Assess for Plasmodium parasites.
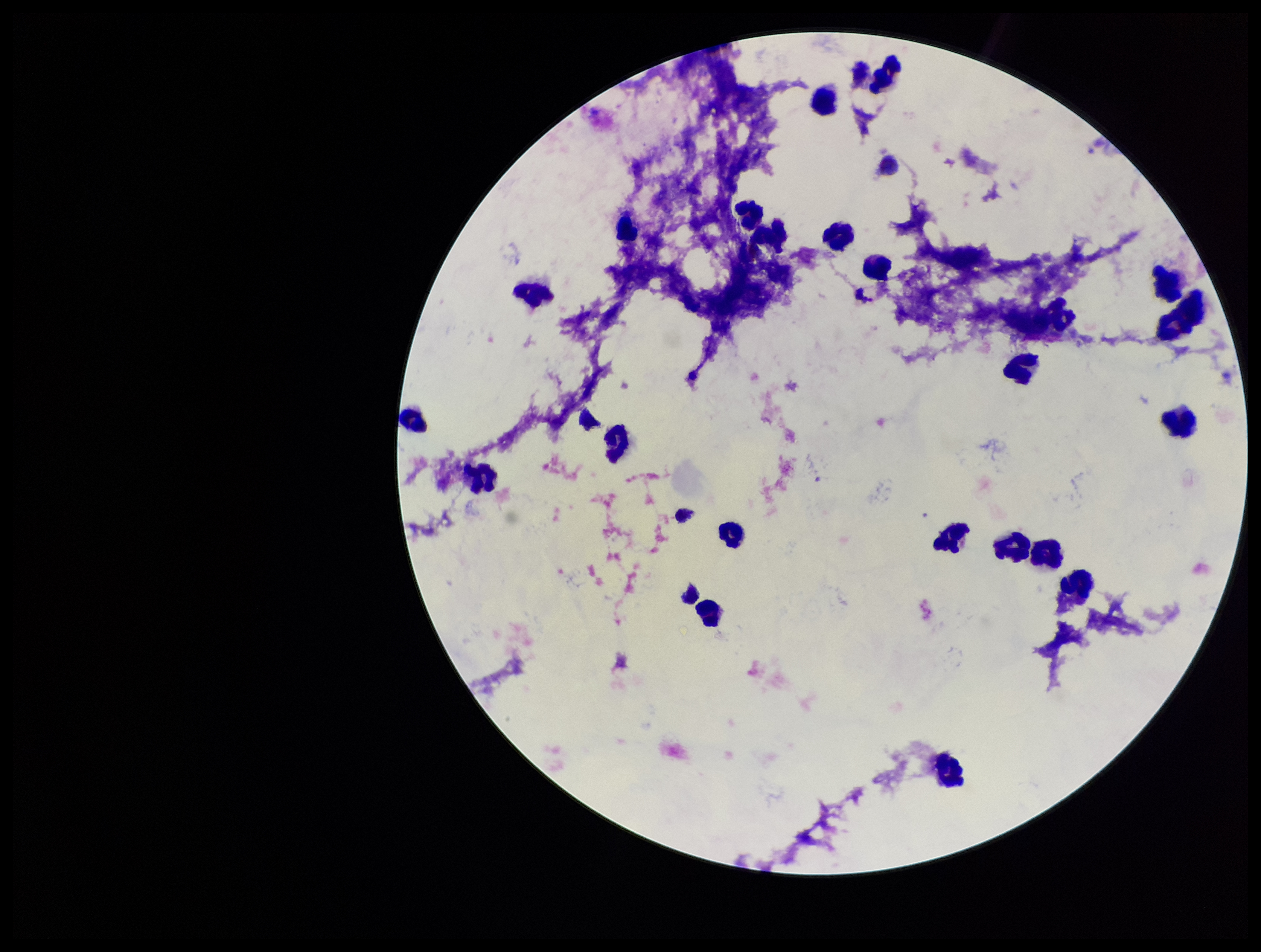

None detected.

Summary:
  - Patient malaria status: infected
  - Species reported for this patient: Plasmodium vivax
  - Leukocyte count: 24
  - Preparation: thick blood smear
  - Stain: Giemsa
  - Capture: smartphone photograph through the microscope eyepiece
  - Parasite count: 0
  - Image size: 1261×952 pixels
  - Field of view: one from this slide